State which cell type is depicted.
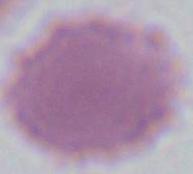
An erythrocyte.

Captured at 1000x magnification. Photomicrograph.